Locate every blood parasite and identify its species.
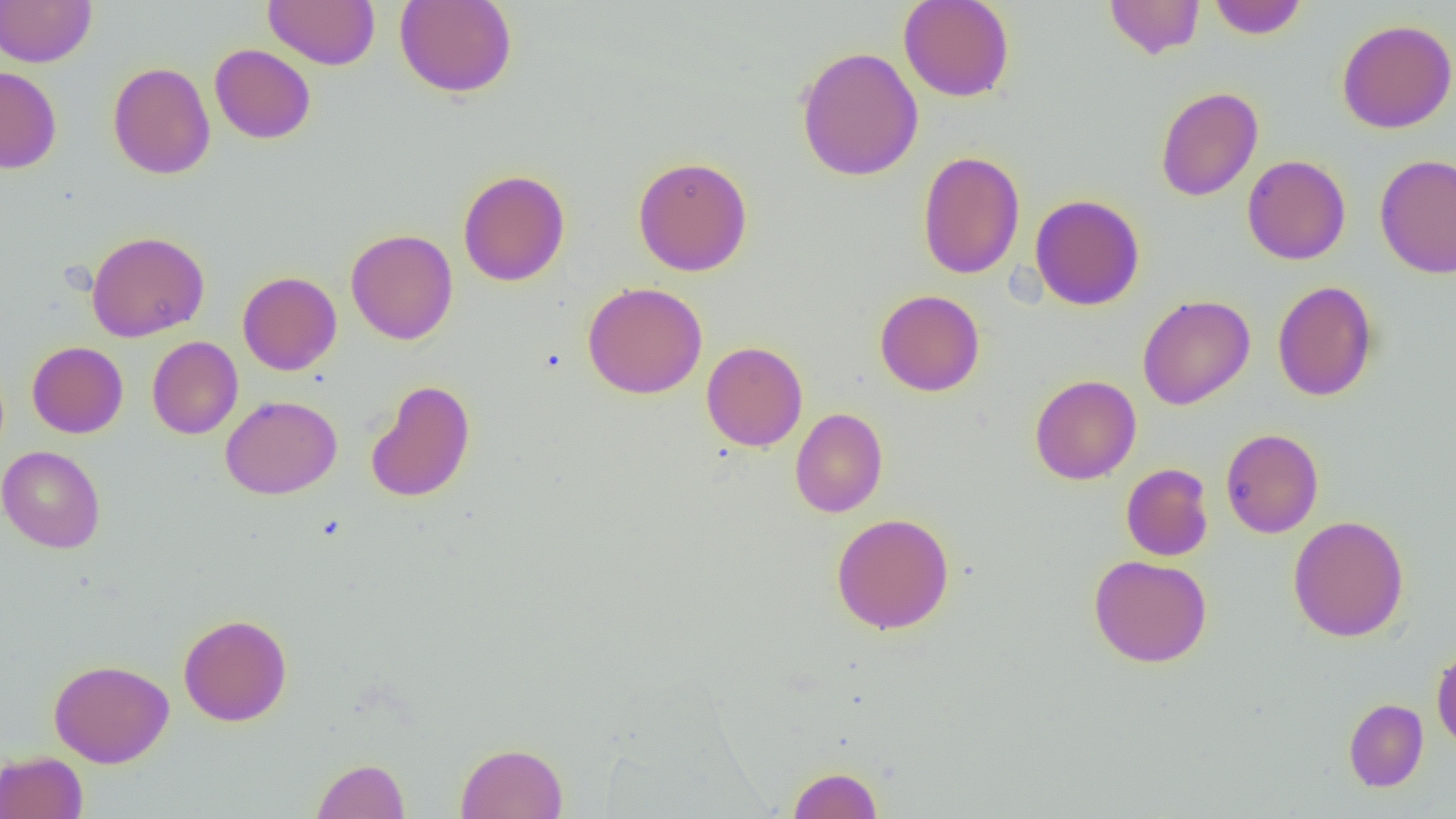
No blood parasites seen.

{
  "slide_level_diagnosis": "no evidence of blood parasites",
  "modality": "light microscopy",
  "field_of_view": "single",
  "image_size": "1456×819 pixels",
  "magnification": "1000x",
  "preparation": "thin blood film",
  "uninfected_red_blood_cell_locations": "approximate bounding boxes as named x1/y1/x2/y2 corners in pixels: (x1=0, y1=0, x2=96, y2=67), (x1=264, y1=0, x2=380, y2=69), (x1=394, y1=0, x2=517, y2=98), (x1=898, y1=0, x2=1015, y2=102), (x1=1105, y1=0, x2=1205, y2=59), (x1=1207, y1=0, x2=1308, y2=39), (x1=1336, y1=19, x2=1456, y2=134), (x1=209, y1=44, x2=316, y2=144), (x1=796, y1=46, x2=923, y2=181), (x1=108, y1=62, x2=216, y2=179), (x1=0, y1=66, x2=62, y2=174), (x1=1155, y1=86, x2=1263, y2=201), (x1=917, y1=150, x2=1025, y2=280), (x1=1374, y1=154, x2=1456, y2=279), (x1=1242, y1=155, x2=1351, y2=265), (x1=633, y1=156, x2=753, y2=276), (x1=458, y1=169, x2=570, y2=286), (x1=1030, y1=194, x2=1145, y2=311), (x1=345, y1=228, x2=458, y2=345), (x1=86, y1=230, x2=210, y2=342), (x1=238, y1=271, x2=342, y2=375), (x1=1272, y1=281, x2=1378, y2=402), (x1=582, y1=282, x2=707, y2=399), (x1=874, y1=290, x2=985, y2=396), (x1=1138, y1=294, x2=1256, y2=410), (x1=147, y1=336, x2=243, y2=439), (x1=701, y1=340, x2=808, y2=451), (x1=27, y1=341, x2=128, y2=438), (x1=1029, y1=374, x2=1141, y2=485), (x1=366, y1=379, x2=475, y2=503), (x1=220, y1=395, x2=342, y2=499), (x1=790, y1=408, x2=888, y2=517), (x1=1221, y1=429, x2=1324, y2=538), (x1=0, y1=445, x2=106, y2=553), (x1=1121, y1=463, x2=1214, y2=561), (x1=831, y1=512, x2=955, y2=635), (x1=1288, y1=515, x2=1409, y2=642), (x1=1088, y1=554, x2=1212, y2=667), (x1=178, y1=613, x2=292, y2=726), (x1=1431, y1=644, x2=1456, y2=754), (x1=49, y1=659, x2=174, y2=768), (x1=1343, y1=698, x2=1428, y2=792), (x1=456, y1=742, x2=568, y2=819), (x1=0, y1=751, x2=88, y2=819), (x1=311, y1=758, x2=410, y2=818), (x1=787, y1=766, x2=883, y2=818)"
}